Assess for Plasmodium parasites.
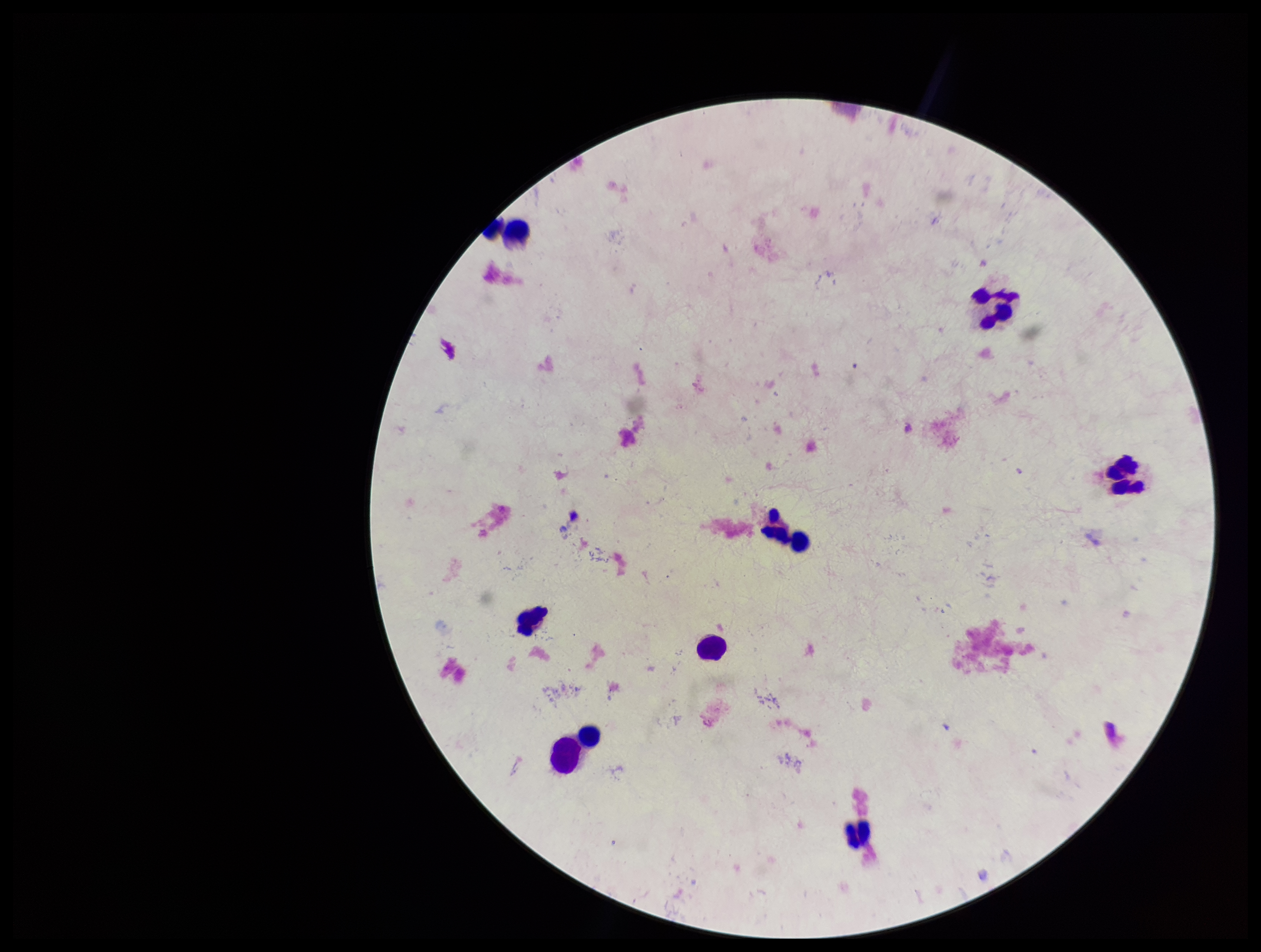
None detected.

Summary:
  - Stain: Giemsa
  - Capture: smartphone photograph through the microscope eyepiece
  - Image size: 1261×952 pixels
  - Preparation: thick smear
  - Field of view: single
  - Parasite count: 0
  - Patient malaria status: negative
  - Leukocyte count: 8